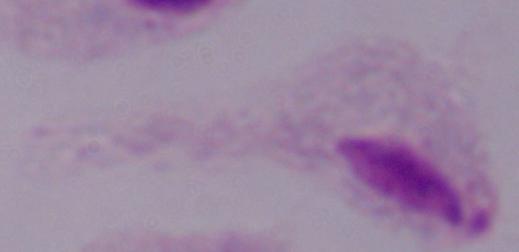
modality: micrograph
identification: trichomonad
magnification: 1000x